State which parasite is depicted.
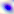

This is Toxoplasma gondii.

400x magnification. Micrograph.